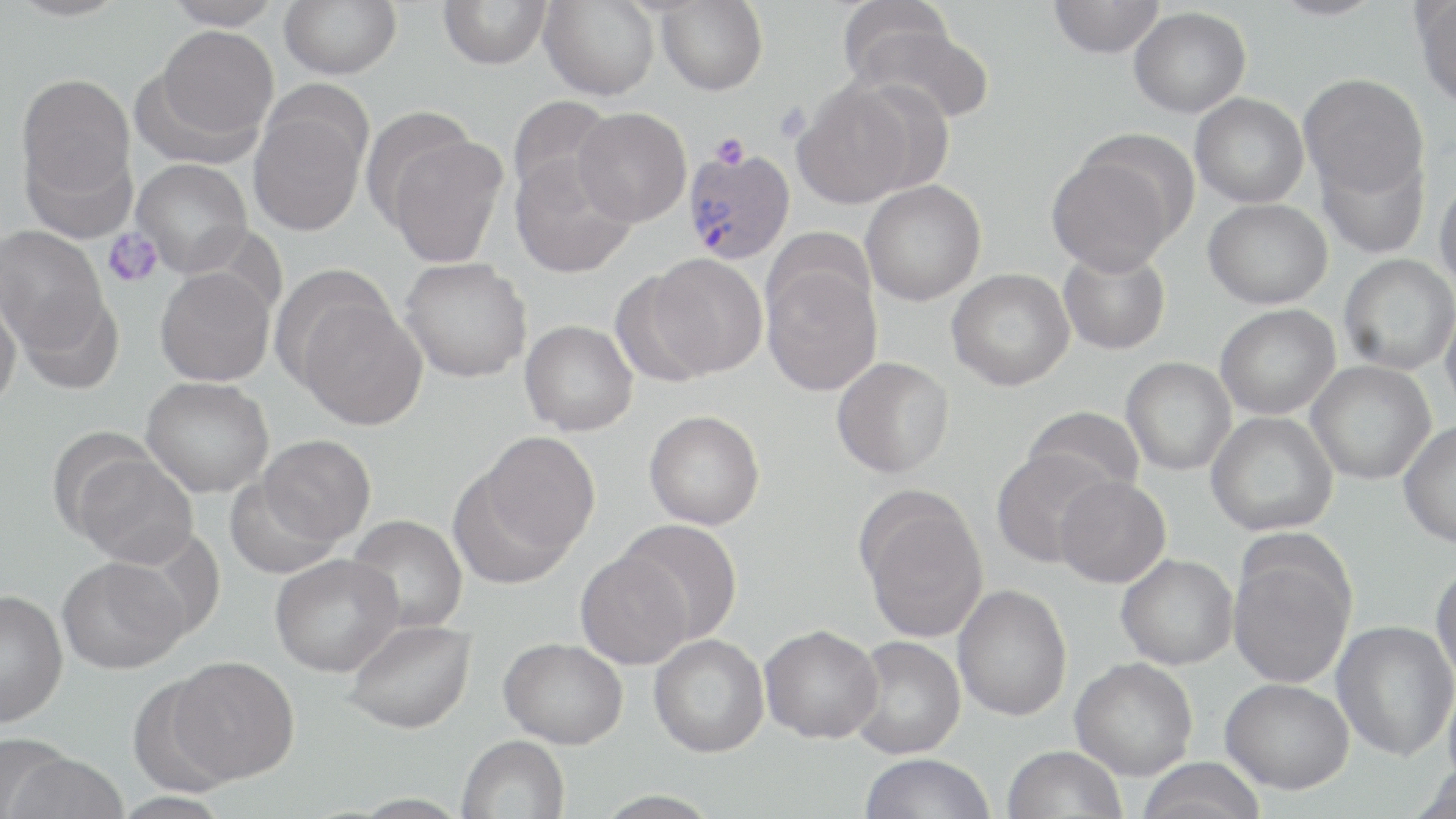

slide-level diagnosis = Plasmodium vivax
stain = May-Grünwald-Giemsa
magnification = 1000x
image size = 1456×819 pixels
modality = optical microscopy
Plasmodium vivax-infected red blood cell locations = approximate bounding boxes as (x1,y1)-(x2,y2) corner pairs in pixels: (680,147)-(795,264)
field of view = single
preparation = thin blood film
platelet locations = approximate bounding boxes as (x1,y1)-(x2,y2) corner pairs in pixels: (773,102)-(813,141), (710,132)-(751,169), (103,228)-(163,288)
uninfected red blood cell locations = approximate bounding boxes as (x1,y1)-(x2,y2) corner pairs in pixels: (161,0)-(284,29), (280,0)-(402,79), (438,0)-(552,69), (835,0)-(956,89), (1047,0)-(1164,58), (1268,0)-(1386,20), (1414,0)-(1456,108), (539,1)-(659,100), (656,1)-(768,96), (1129,6)-(1251,118), (848,23)-(995,124), (151,25)-(279,146), (15,73)-(136,220), (1299,73)-(1429,198), (790,79)-(924,208), (1190,93)-(1309,208), (507,95)-(616,205), (248,96)-(370,238), (360,105)-(478,229), (573,108)-(691,226), (382,133)-(507,268), (1314,142)-(1430,259), (1045,148)-(1181,276), (510,155)-(637,279), (132,159)-(253,276), (1434,175)-(1456,293), (860,180)-(986,306), (1203,198)-(1332,309), (0,225)-(108,355), (1059,247)-(1170,355), (645,253)-(768,378), (1339,253)-(1455,375), (399,258)-(532,382), (761,261)-(883,396), (273,263)-(400,390), (154,268)-(275,387), (946,268)-(1075,391), (608,272)-(717,387), (13,289)-(124,396), (0,290)-(22,410), (1441,297)-(1456,422), (294,298)-(427,431), (1215,304)-(1340,420), (519,320)-(638,436), (831,357)-(954,478), (1121,357)-(1236,476), (1305,360)-(1435,484), (141,377)-(274,497), (1022,406)-(1145,500), (644,410)-(765,530), (1206,411)-(1338,536), (1398,420)-(1456,547), (470,431)-(600,567), (258,435)-(375,546), (991,448)-(1118,569), (71,450)-(198,568), (1054,475)-(1171,588), (224,476)-(341,580), (857,489)-(988,643), (345,514)-(468,634), (617,519)-(743,645), (1227,547)-(1355,689), (575,550)-(692,669), (270,553)-(403,677), (1116,553)-(1239,670), (57,555)-(190,674), (1430,561)-(1456,687), (953,584)-(1072,721), (0,589)-(68,727), (344,619)-(476,734), (1331,620)-(1456,761), (760,624)-(883,743), (649,634)-(769,757), (847,636)-(966,759), (499,637)-(628,748), (166,655)-(300,784), (1070,657)-(1198,780), (125,676)-(238,797), (1220,677)-(1354,794), (1443,679)-(1456,795), (457,735)-(569,819), (1001,745)-(1127,819), (5,749)-(129,819), (859,753)-(995,819), (1135,757)-(1269,819), (1408,763)-(1456,819), (592,789)-(724,817), (109,791)-(234,819)